State which cell type is depicted.
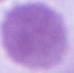

An erythrocyte.

Summary:
  - Modality: photomicrograph
  - Magnification: 1000x